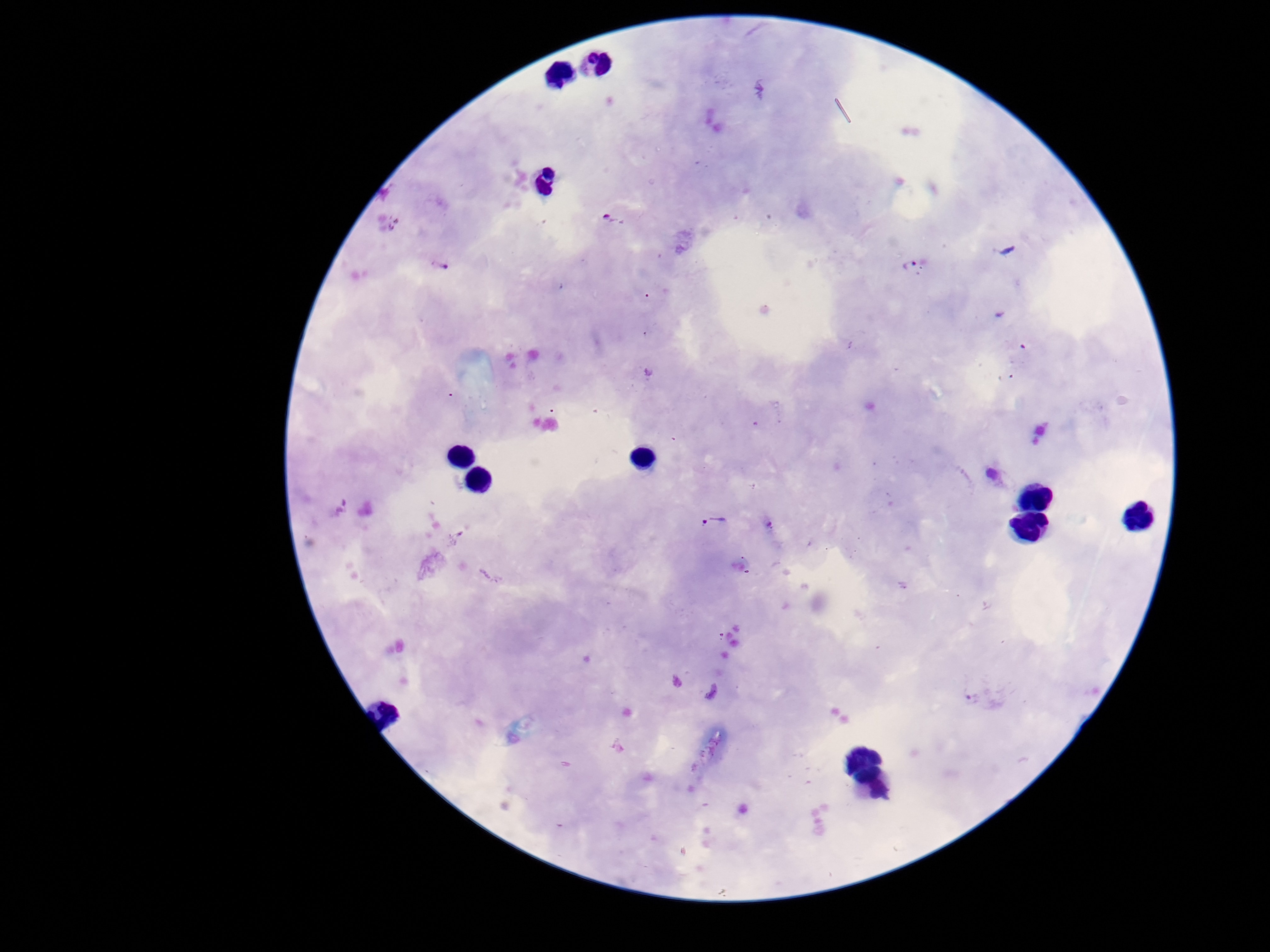

Approximate centers as [x, y] in pixels.
Summary:
  - Plasmodium parasite locations: [611, 220], [912, 265], [438, 266], [995, 477], [718, 524], [972, 699]
  - Patient malaria status: infected
  - Magnification: 100x
  - Capture: smartphone camera through the microscope eyepiece
  - Field of view: one from this slide
  - Image size: 1270×952 pixels
  - Stain: Giemsa
  - Preparation: thick peripheral-blood smear